Identify the cell.
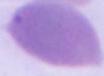

This is an erythrocyte.

Captured at 1000x magnification. Photomicrograph.